State which parasite is depicted.
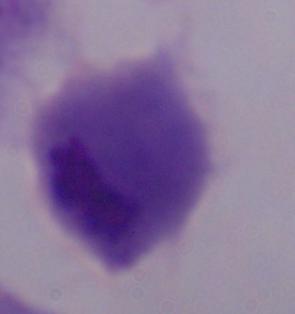

This is a trichomonad.

modality = photomicrograph
magnification = 1000x